Classify this cell by malaria status.
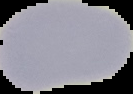
It is uninfected.

image type = segmented cell region with the area outside set to black
image size = 133×94 pixels
preparation = thin blood film